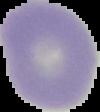
Summary:
  - Image size: 100×112 pixels
  - Preparation: thin blood smear
  - Image type: cell region segmented out of the field of view; surrounding area masked to black
  - Malaria status: uninfected